Report the malaria status of this cell.
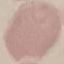
Uninfected.

{
  "capture": "smartphone through the microscope eyepiece",
  "image_type": "cell patch, automatically extracted from a larger field of view and resized to 64 × 64 pixels",
  "preparation": "thin blood smear",
  "stain": "Giemsa"
}